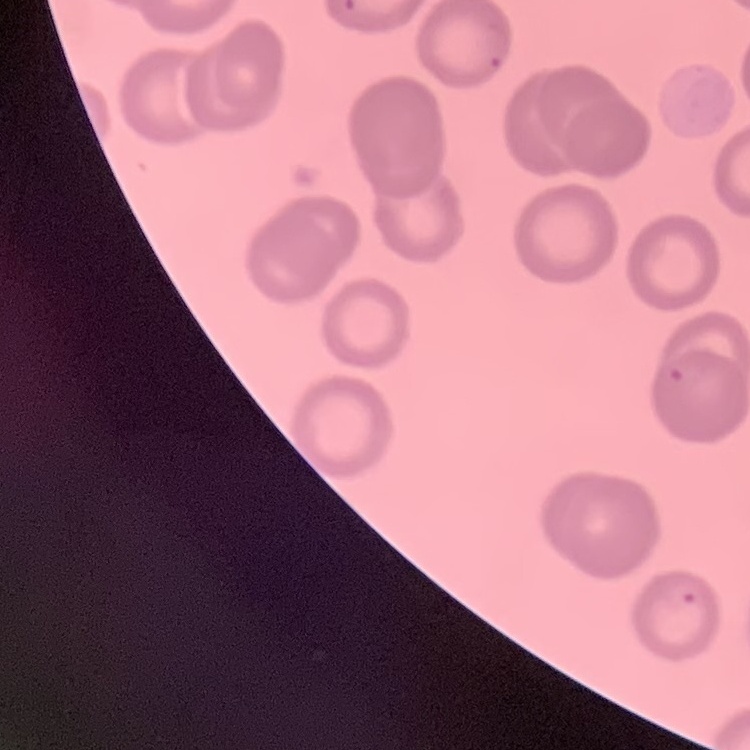

Summary:
  - Red blood cell morphology: no rouleaux formation
  - Image type: square crop of a larger photomicrograph
  - Stain: Field's or Giemsa
  - Preparation: thin peripheral smear